Assess this cell for malaria.
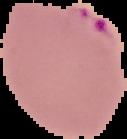
Parasitized.

Summary:
  - Preparation: thin blood film
  - Image type: segmented cell region on a black background
  - Image size: 127×139 pixels